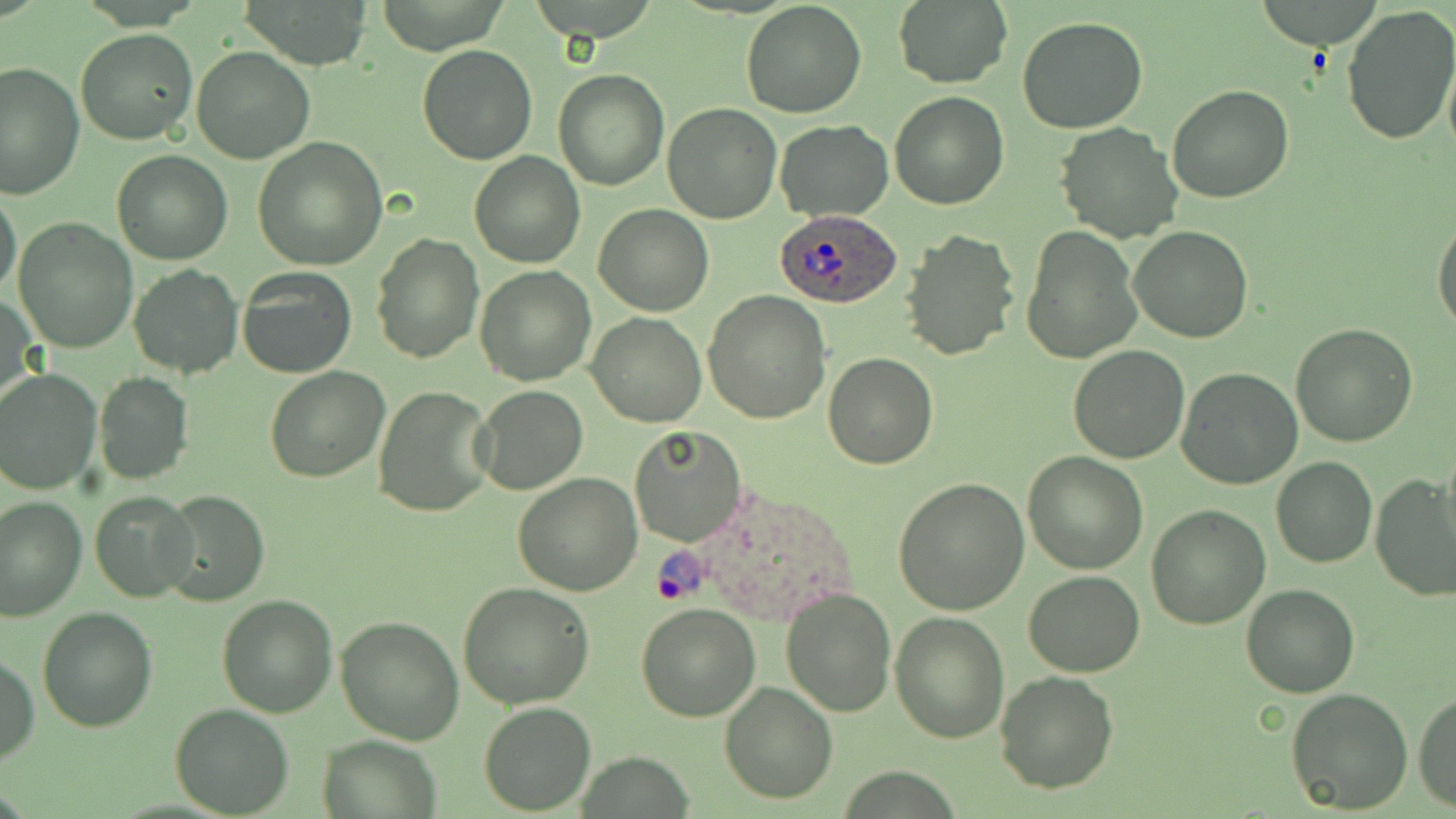

slide-level diagnosis = Plasmodium ovale
field of view = one of a larger specimen
image size = 1456×819 pixels
uninfected red blood cell locations = approximate bounding boxes as [x1, y1, x2, y2] in pixels: [238, 0, 375, 68], [1258, 0, 1385, 49], [740, 1, 866, 118], [893, 1, 1012, 87], [1339, 4, 1456, 146], [1017, 15, 1149, 133], [76, 29, 199, 146], [418, 44, 538, 164], [191, 45, 315, 163], [1442, 52, 1456, 164], [0, 61, 84, 199], [553, 68, 668, 190], [1167, 84, 1294, 203], [889, 91, 1008, 210], [662, 102, 781, 223], [773, 120, 892, 221], [1054, 123, 1183, 243], [251, 137, 388, 269], [112, 149, 233, 264], [469, 150, 585, 269], [0, 190, 23, 301], [591, 204, 713, 316], [1432, 215, 1456, 340], [12, 218, 139, 353], [1021, 225, 1141, 366], [1129, 227, 1254, 343], [898, 228, 1020, 362], [371, 233, 483, 364], [128, 265, 243, 379], [474, 265, 596, 386], [238, 267, 357, 379], [703, 291, 831, 425], [2, 294, 38, 412], [587, 311, 706, 427], [1289, 323, 1418, 447], [1067, 346, 1191, 464], [824, 354, 937, 471], [263, 366, 390, 483], [1176, 367, 1303, 489], [0, 368, 102, 494], [93, 372, 194, 486], [473, 384, 589, 496], [372, 385, 494, 519], [629, 426, 745, 548], [1438, 447, 1456, 566], [1022, 451, 1149, 574], [1271, 457, 1376, 568], [513, 471, 643, 594], [1370, 472, 1455, 600], [894, 476, 1030, 614], [158, 489, 270, 607], [90, 490, 198, 602], [0, 496, 87, 621], [1146, 505, 1270, 629], [1024, 570, 1145, 676], [457, 582, 595, 709], [1240, 582, 1361, 698], [781, 586, 897, 717], [217, 594, 339, 715], [637, 602, 762, 721], [37, 608, 157, 732], [890, 610, 1010, 742], [335, 615, 465, 745], [1, 656, 38, 765], [994, 671, 1119, 793], [719, 680, 837, 803], [1285, 686, 1414, 814], [1414, 690, 1455, 811], [480, 703, 596, 814], [170, 704, 296, 817], [318, 735, 441, 818]
modality = light microscopy
stain = May-Grünwald-Giemsa
preparation = thin blood film
magnification = 1000x
Plasmodium ovale-infected red blood cell locations = approximate bounding boxes as [x1, y1, x2, y2] in pixels: [775, 205, 898, 307], [646, 487, 863, 623]